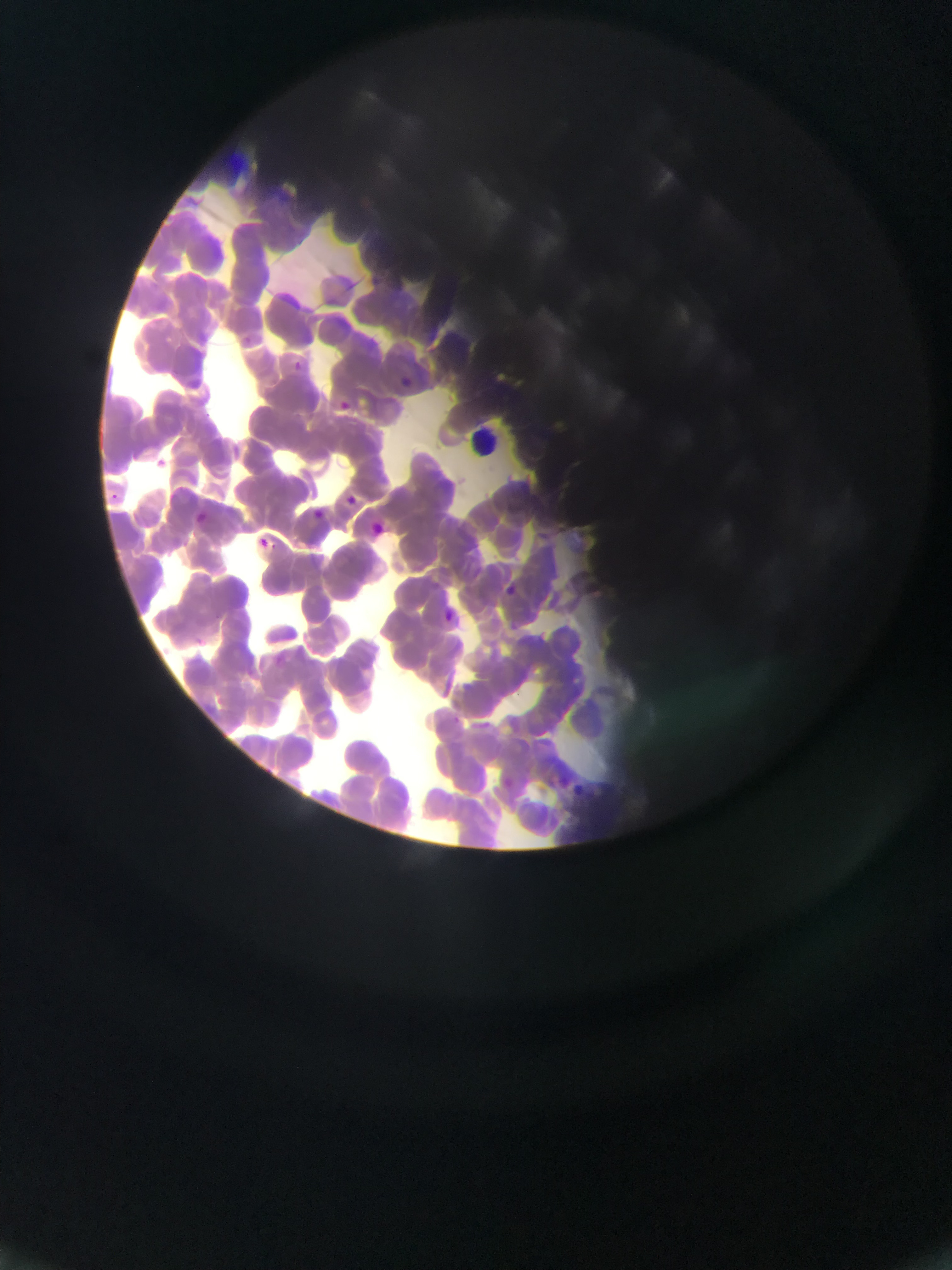
image size = 952×1270 pixels
capture = mobile-phone photograph through a microscope
field of view = single
malaria parasite locations = approximate bounding boxes as left top right bottom in pixels: 287 358 306 376; 403 372 417 384; 328 397 353 418; 340 491 361 510; 308 507 327 524; 195 508 221 526; 364 519 389 542; 260 533 269 546; 492 583 521 602; 439 609 460 627; 506 620 522 634; 559 774 568 783
preparation = thin blood film
country = Ghana